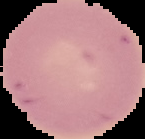 Image is 145×139 pixels. From a thin blood film. Result: no Plasmodium parasites detected. Segmented cell region on a black background.